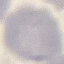

Malaria status: uninfected. Acquired by smartphone through the microscope eyepiece. Giemsa stain. Thin blood film. Cell patch, automatically extracted from a larger field of view and resized to 64 × 64 pixels.